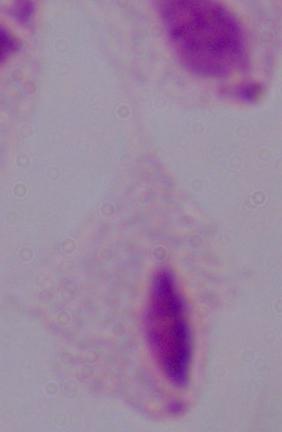 A trichomonad is seen. 1000x magnification. Micrograph.